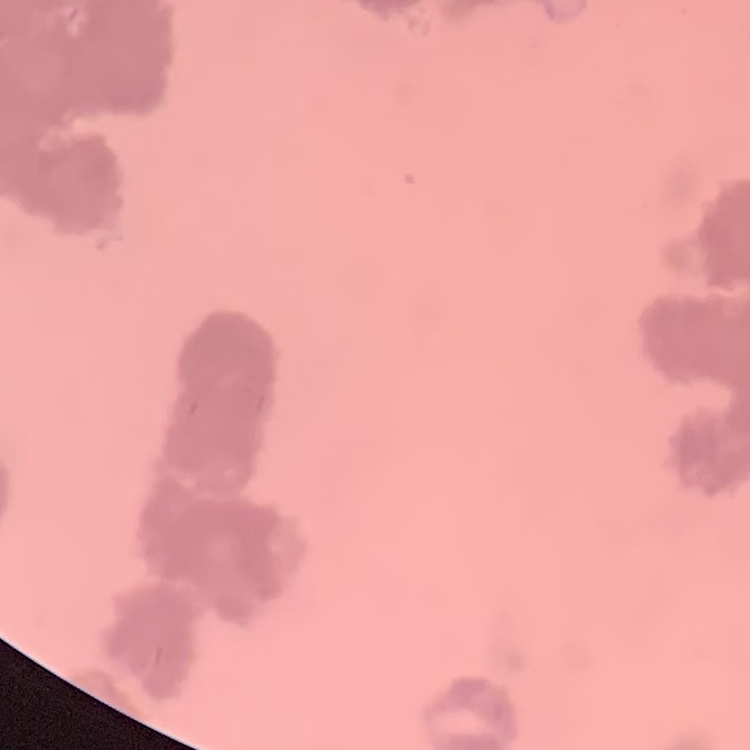

The erythrocytes exhibit rouleaux formation. Thin blood film. Stained with either Field's or Giemsa. Square crop of a larger photomicrograph.